Name the parasite shown.
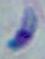
This is Toxoplasma gondii.

modality = photomicrograph
magnification = 1000x